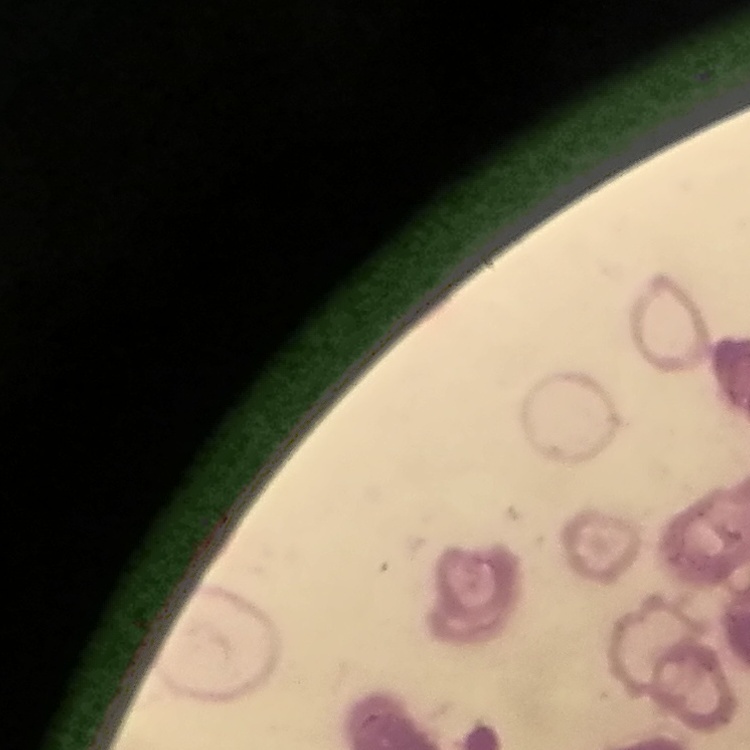
{
  "red_blood_cell_morphology": "rouleaux formation",
  "stain": "Field's or Giemsa",
  "image_type": "square crop of a larger photomicrograph",
  "preparation": "thin peripheral smear"
}